Locate and identify every blood parasite.
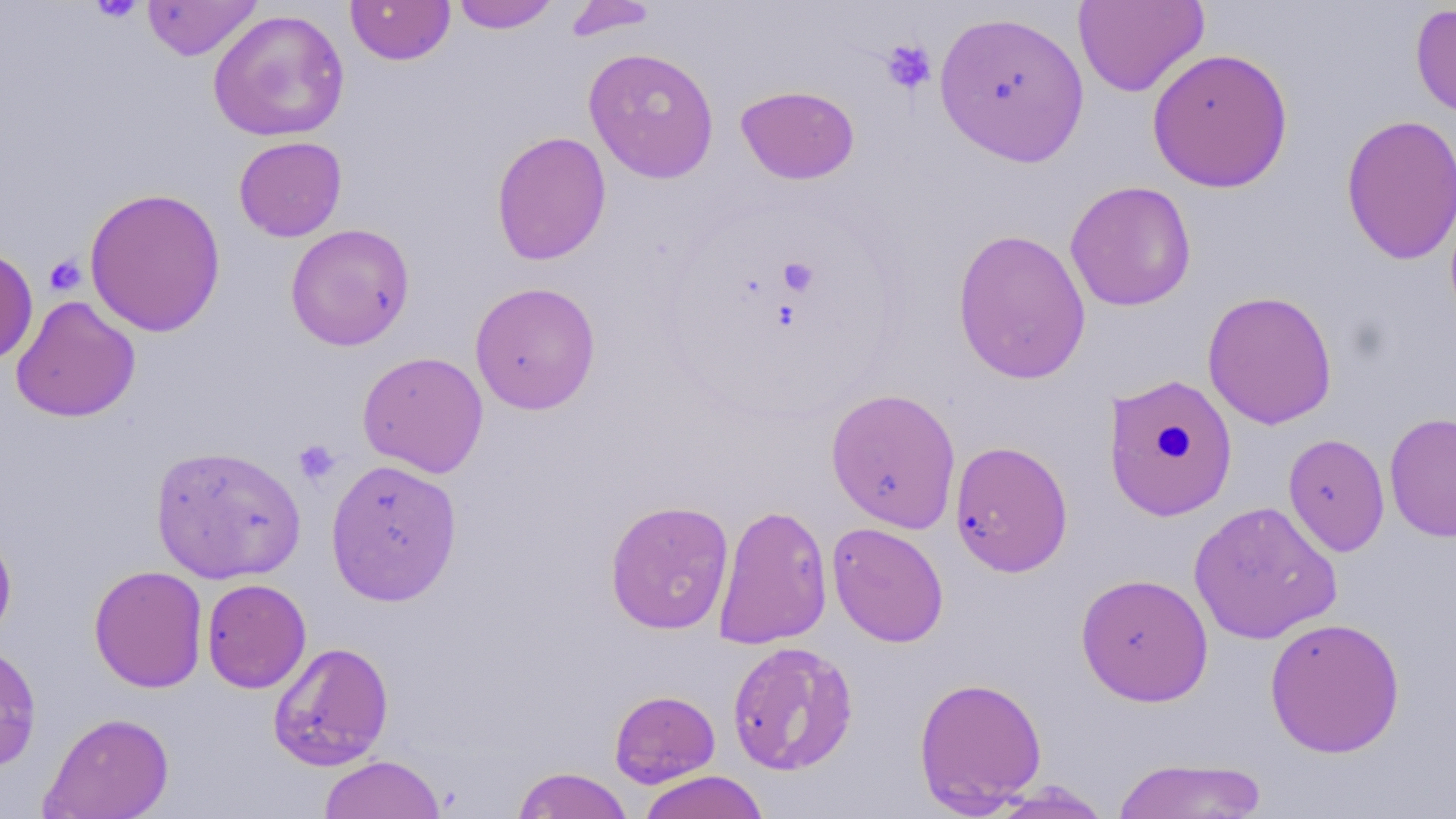

No blood parasites seen.

{
  "slide_level_diagnosis": "no evidence of blood parasites",
  "preparation": "thin blood film",
  "stain": "May-Grünwald-Giemsa",
  "magnification": "1000x",
  "modality": "light microscopy",
  "uninfected_red_blood_cell_locations": "approximate bounding boxes as (x1,y1)-(x2,y2) corner pairs in pixels: (142,0)-(262,61), (345,0)-(455,66), (450,0)-(562,33), (562,1)-(659,41), (1073,1)-(1209,98), (1410,4)-(1456,122), (208,9)-(350,142), (933,9)-(1090,166), (583,47)-(720,183), (1146,48)-(1293,192), (736,85)-(860,184), (1340,113)-(1456,265), (491,131)-(612,266), (233,136)-(347,241), (1064,180)-(1196,311), (84,186)-(227,338), (285,223)-(415,351), (952,228)-(1091,385), (0,246)-(38,365), (469,281)-(601,415), (1202,290)-(1338,430), (11,296)-(140,422), (357,351)-(489,478), (1102,373)-(1239,522), (825,387)-(961,533), (1384,412)-(1456,542), (1282,433)-(1390,556), (949,440)-(1074,577), (150,444)-(306,584), (325,458)-(463,605), (604,499)-(735,635), (1188,500)-(1343,645), (713,503)-(833,650), (826,522)-(950,647), (0,525)-(17,645), (89,564)-(208,693), (1075,572)-(1214,707), (201,578)-(312,693), (1264,616)-(1405,758), (268,641)-(394,770), (726,641)-(858,775), (0,643)-(42,771), (913,676)-(1047,814), (609,689)-(720,788), (40,712)-(175,819), (319,754)-(446,818), (1112,757)-(1269,818), (511,767)-(634,819), (638,770)-(770,819), (983,782)-(1114,818)",
  "image_size": "1456×819 pixels",
  "platelet_locations": "approximate bounding boxes as (x1,y1)-(x2,y2) corner pairs in pixels: (90,0)-(145,23), (880,38)-(937,94), (44,254)-(86,296), (778,258)-(819,296), (293,439)-(341,487)",
  "field_of_view": "one of a larger specimen"
}